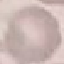

Malaria status: uninfected. Acquired by smartphone through the microscope eyepiece. Giemsa stain. Cell patch, automatically extracted from a larger field of view and resized to 64 × 64 pixels. Thin smear of blood.